Classify this cell by malaria status.
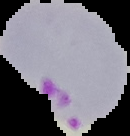

Parasitized.

preparation = thin blood film
image size = 130×136 pixels
image type = segmented cell region with the area outside set to black